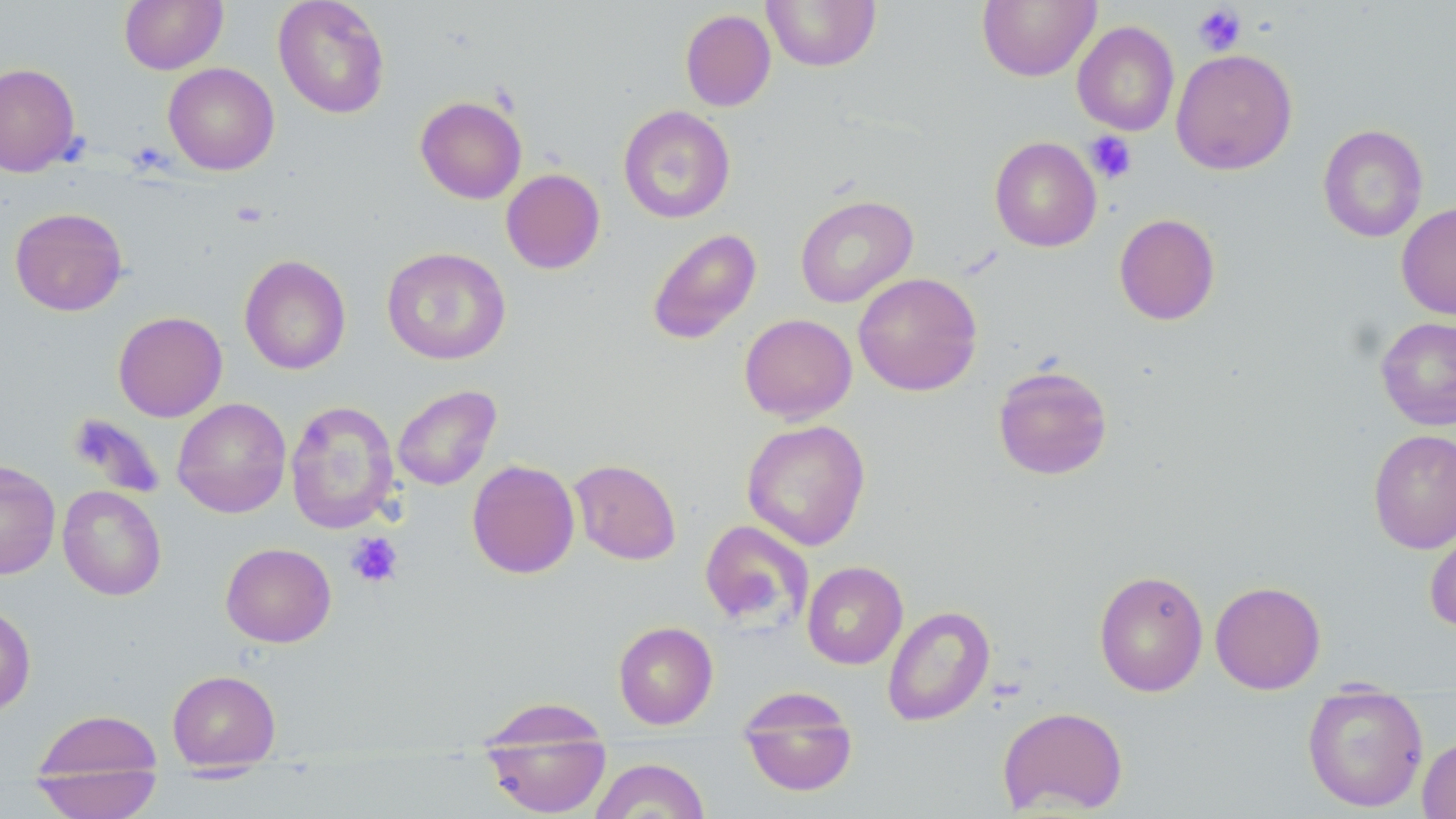

slide_level_diagnosis: no evidence of blood parasites
modality: optical microscopy
magnification: 1000x
stain: May-Grünwald-Giemsa
platelet_locations_subset: 'approximate bounding boxes as (x1,y1)-(x2,y2) corner pairs in pixels: (1191,4)-(1247,56), (1085,131)-(1137,183), (346,532)-(403,588)'
field_of_view: one of a larger specimen
preparation: thin blood film
image_size: 1456×819 pixels
uninfected_red_blood_cell_locations_subset: 'approximate bounding boxes as (x1,y1)-(x2,y2) corner pairs in pixels: (119,0)-(227,74), (273,0)-(391,119), (761,0)-(881,71), (977,0)-(1100,82), (680,9)-(776,111), (1072,21)-(1179,136), (1171,49)-(1298,175), (163,62)-(279,175), (0,63)-(81,177), (415,96)-(527,204), (618,105)-(736,224), (1317,124)-(1429,242), (990,136)-(1102,252), (501,168)-(605,274), (795,194)-(917,308), (1396,202)-(1456,320), (10,207)-(128,316), (1114,213)-(1221,325), (647,228)-(762,344), (381,247)-(511,365), (239,254)-(351,375), (853,272)-(982,396), (113,311)-(228,422), (739,313)-(857,424), (1376,316)-(1456,431), (992,364)-(1113,480), (392,384)-(502,490), (172,397)-(291,518), (285,400)-(399,534), (742,420)-(870,551), (1368,429)-(1456,554), (466,459)-(580,579), (569,459)-(682,565), (0,460)-(61,580), (57,485)-(167,600), (699,520)-(814,630), (1424,523)-(1456,633), (220,542)-(336,648), (802,561)-(908,669), (1094,569)-(1209,697), (1210,580)-(1326,694), (0,602)-(36,718), (882,605)-(995,726), (613,621)-(718,729), (167,669)-(281,770), (737,686)-(859,798), (1301,691)-(1429,813), (997,706)-(1129,816), (31,709)-(163,787), (480,712)-(612,819), (1417,734)-(1456,818), (588,757)-(710,819), (30,767)-(164,818)'